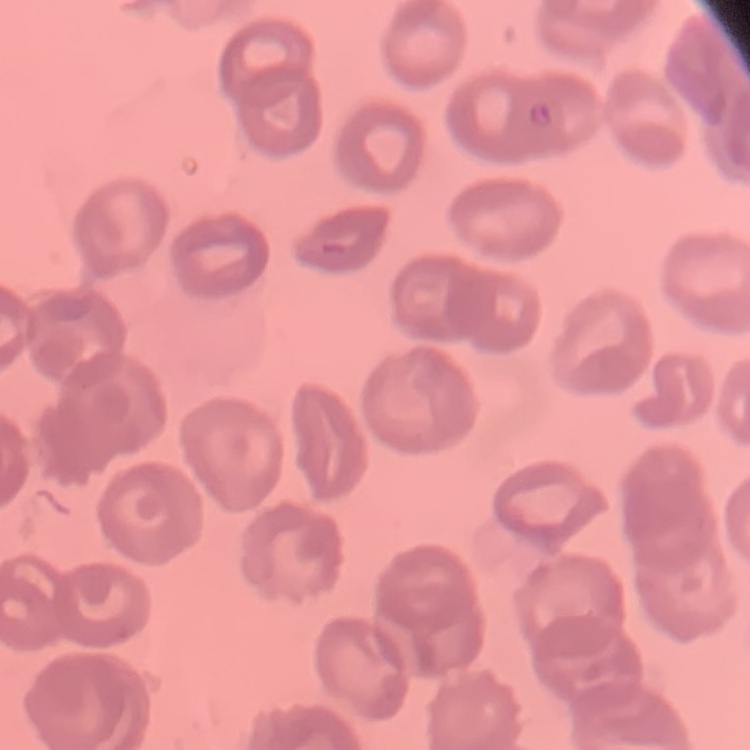
The red blood cells exhibit no rouleaux formation. Field's or Giemsa stain. Square crop of a larger photomicrograph. Thin blood smear.